Locate every blood parasite and identify its species.
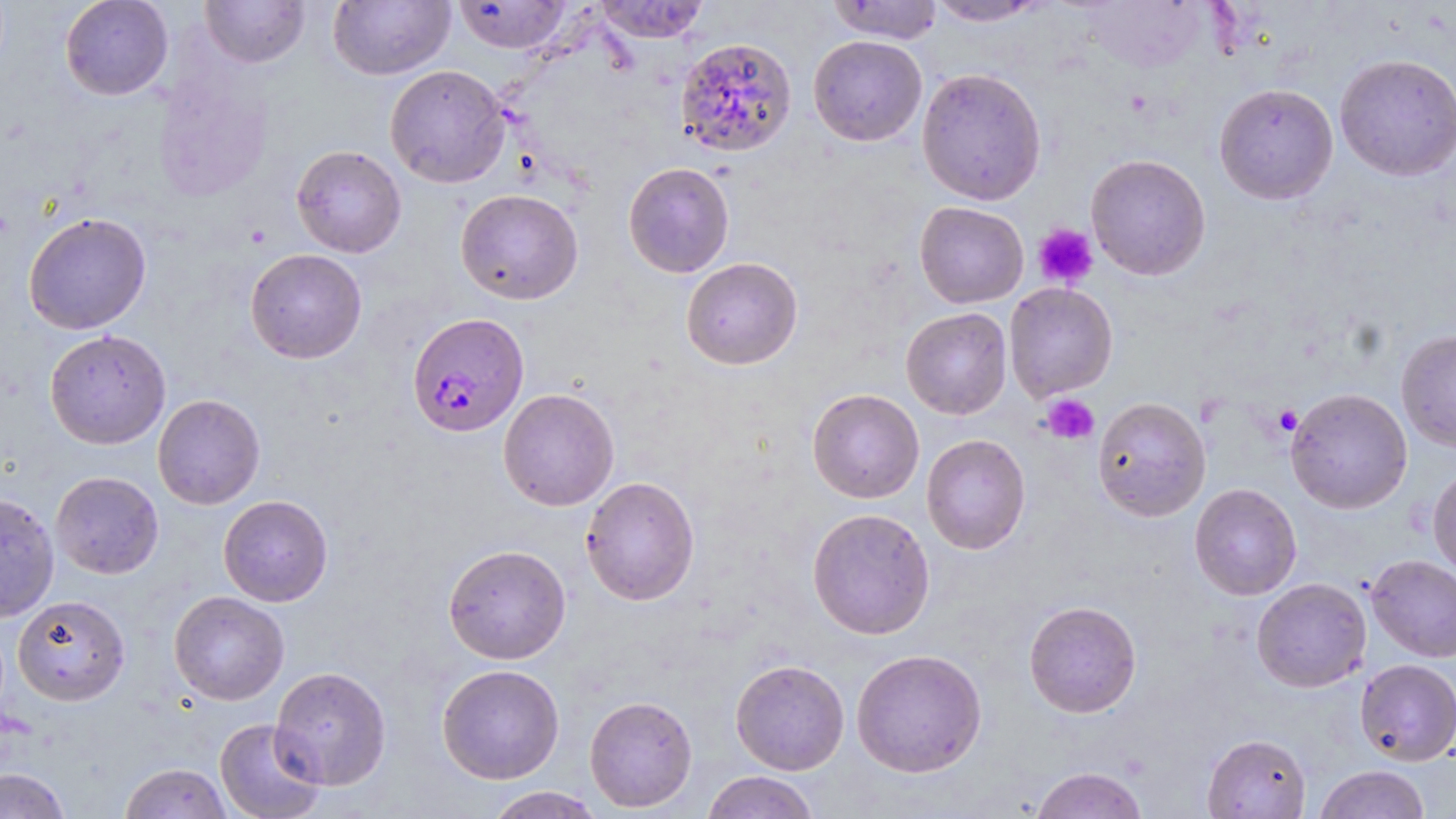
Approximate bounding boxes as [x1, y1, x2, y2] in pixels.
Plasmodium falciparum-infected red blood cells: [407, 312, 529, 438].
No Plasmodium ovale, Plasmodium malariae, Plasmodium vivax, Babesia divergens, or Trypanosoma brucei observed.

Summary:
  - Platelet locations: [1033, 223, 1098, 289], [1042, 393, 1099, 445], [1272, 405, 1302, 437]
  - Uninfected red blood cell locations: [60, 0, 173, 100], [199, 0, 310, 68], [593, 0, 711, 43], [826, 0, 945, 44], [926, 0, 1052, 27], [328, 1, 454, 80], [453, 1, 573, 53], [1077, 1, 1212, 74], [808, 35, 928, 146], [675, 37, 798, 158], [1334, 52, 1456, 181], [385, 64, 510, 188], [916, 67, 1047, 205], [153, 71, 273, 202], [1214, 83, 1339, 204], [291, 145, 407, 258], [1086, 153, 1211, 280], [623, 161, 735, 278], [455, 189, 583, 305], [915, 201, 1029, 308], [23, 212, 152, 335], [245, 248, 367, 364], [681, 257, 803, 370], [1004, 282, 1118, 402], [900, 307, 1012, 420], [1396, 328, 1456, 452], [43, 329, 171, 449], [498, 388, 619, 511], [807, 388, 924, 503], [1285, 388, 1412, 513], [152, 393, 265, 509], [1092, 396, 1212, 522], [921, 434, 1031, 555], [1428, 464, 1456, 581], [50, 471, 164, 579], [581, 476, 700, 606], [1189, 483, 1302, 600], [0, 493, 59, 623], [218, 495, 333, 607], [806, 507, 935, 639], [442, 544, 571, 664], [1365, 554, 1456, 662], [1251, 577, 1371, 692], [168, 590, 289, 705], [12, 595, 130, 706], [1023, 600, 1141, 718], [851, 648, 987, 778], [1355, 658, 1456, 765], [730, 659, 849, 775], [436, 664, 565, 784], [270, 665, 392, 790], [584, 695, 697, 812], [214, 718, 326, 819], [1202, 733, 1311, 818], [119, 762, 234, 819], [1314, 765, 1430, 819], [1030, 767, 1149, 818], [0, 768, 71, 818], [701, 770, 820, 819], [484, 786, 605, 818]
  - Slide-level diagnosis: Plasmodium falciparum
  - Preparation: thin blood smear
  - Image size: 1456×819 pixels
  - Modality: optical microscopy
  - Stain: May-Grünwald-Giemsa
  - Field of view: single
  - Magnification: 1000x